Report the malaria status of this cell.
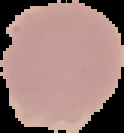
It is uninfected.

From a thin blood smear. Cell region segmented out of the field of view; the surrounding area is masked to black. Image is 124×133 pixels.